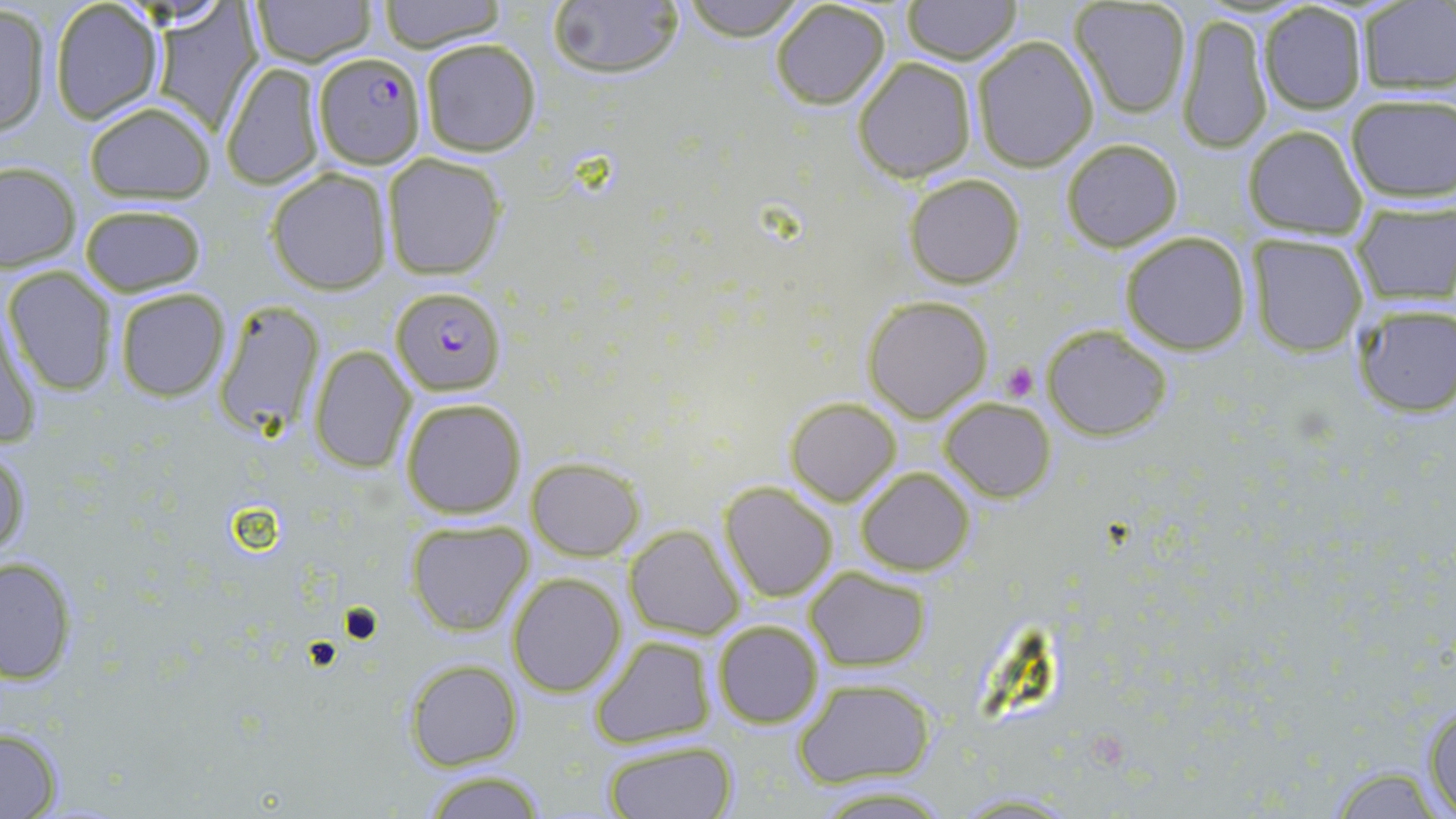

slide-level diagnosis = Plasmodium falciparum
preparation = thin blood smear
field of view = one of a larger specimen
uninfected red blood cell locations = approximate bounding boxes as (x1, y1, x2, y2) in pixels: (251, 0, 374, 66), (376, 0, 507, 53), (545, 0, 686, 85), (678, 0, 810, 41), (901, 0, 1021, 63), (768, 1, 892, 111), (1068, 1, 1193, 119), (50, 2, 163, 126), (1256, 2, 1370, 115), (1358, 2, 1456, 96), (146, 3, 269, 135), (1, 6, 52, 137), (1176, 10, 1274, 153), (970, 35, 1098, 173), (419, 37, 540, 157), (852, 57, 977, 182), (222, 63, 324, 190), (1345, 95, 1456, 203), (84, 99, 218, 207), (1241, 125, 1369, 239), (1059, 137, 1185, 253), (383, 152, 505, 280), (1, 163, 79, 272), (265, 167, 391, 294), (905, 173, 1026, 288), (1351, 199, 1456, 304), (79, 203, 206, 297), (1120, 231, 1251, 353), (1244, 234, 1369, 357), (5, 265, 120, 396), (113, 287, 230, 402), (863, 296, 995, 423), (212, 299, 327, 438), (0, 302, 42, 451), (1349, 302, 1456, 416), (1042, 323, 1173, 440), (308, 345, 414, 473), (784, 396, 902, 506), (940, 396, 1055, 501), (399, 397, 528, 520), (1, 440, 33, 566), (528, 458, 643, 561), (856, 466, 975, 576), (718, 481, 838, 601), (405, 519, 533, 636), (625, 524, 745, 640), (0, 555, 79, 685), (805, 568, 931, 671), (508, 572, 628, 696), (712, 620, 824, 730), (590, 635, 716, 749), (406, 660, 523, 769), (792, 678, 936, 787), (1422, 698, 1456, 819), (0, 726, 64, 817), (601, 738, 738, 818), (1323, 763, 1447, 818), (416, 770, 554, 818)
stain = May-Grünwald-Giemsa
modality = optical microscopy
image size = 1456×819 pixels
Plasmodium falciparum-infected red blood cell locations = approximate bounding boxes as (x1, y1, x2, y2) in pixels: (312, 50, 423, 166), (391, 285, 505, 398)
platelet locations = approximate bounding boxes as (x1, y1, x2, y2) in pixels: (1002, 362, 1040, 402)
magnification = 1000x